Outline each blood parasite and name the species.
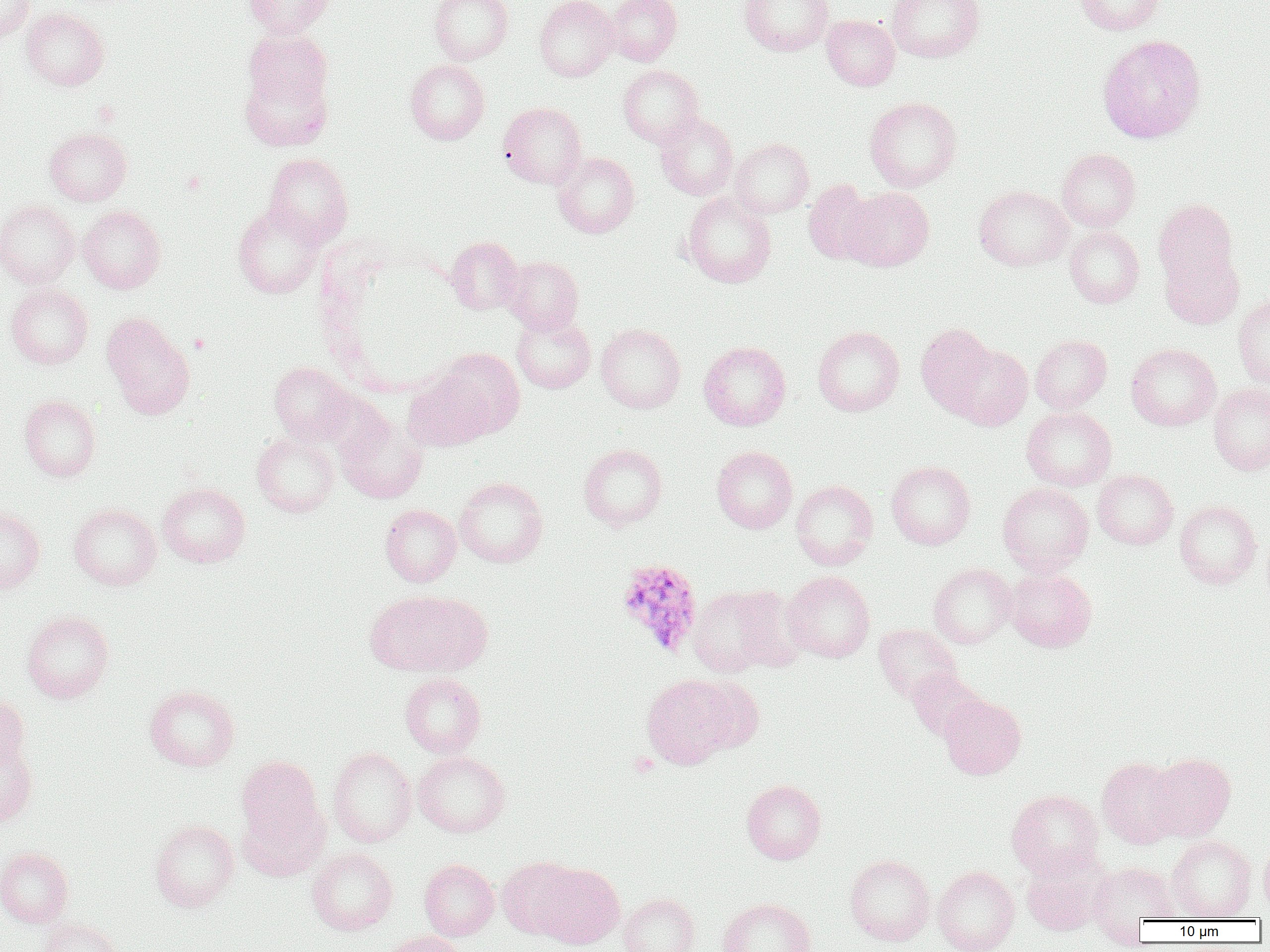
Approximate bounding boxes as (x1,y1)-(x2,y2) corner pairs in pixels.
Plasmodium ovale-infected red blood cells: (617,561)-(704,658).
No Plasmodium falciparum, Plasmodium malariae, Plasmodium vivax, Babesia divergens, or Trypanosoma brucei observed.

{
  "slide_level_diagnosis": "Plasmodium ovale",
  "uninfected_red_blood_cell_locations": "approximate bounding boxes as (x1,y1)-(x2,y2) corner pairs in pixels: (0,0)-(34,41), (244,0)-(332,38), (429,0)-(513,64), (534,0)-(618,81), (605,0)-(682,65), (739,0)-(833,55), (886,0)-(985,62), (1076,0)-(1166,35), (20,7)-(110,91), (822,15)-(899,90), (1097,34)-(1206,143), (405,59)-(490,144), (239,64)-(333,151), (618,64)-(703,147), (865,96)-(962,192), (498,102)-(587,188), (654,112)-(739,200), (44,127)-(132,206), (729,138)-(814,218), (1057,149)-(1140,231), (553,152)-(640,238), (264,153)-(353,245), (803,179)-(877,264), (974,185)-(1073,271), (842,186)-(934,271), (681,192)-(776,287), (1153,199)-(1239,291), (0,200)-(79,288), (233,203)-(323,298), (78,205)-(166,294), (1065,226)-(1144,308), (446,236)-(523,314), (1160,250)-(1243,329), (502,256)-(583,334), (6,283)-(93,369), (1233,294)-(1270,388), (102,313)-(195,418), (511,313)-(595,393), (596,323)-(685,413), (915,323)-(997,416), (813,326)-(904,416), (1030,334)-(1111,413), (698,340)-(791,430), (949,343)-(1032,430), (1126,343)-(1220,430), (435,348)-(525,438), (269,362)-(354,444), (403,371)-(492,451), (1209,383)-(1270,475), (18,395)-(101,481), (1022,407)-(1117,490), (336,414)-(427,503), (252,431)-(339,517), (578,443)-(667,530), (711,446)-(797,533), (886,461)-(976,549), (1093,469)-(1178,549), (454,476)-(548,568), (791,480)-(878,569), (158,482)-(250,567), (998,483)-(1093,575), (1174,500)-(1262,588), (69,502)-(161,590), (380,504)-(461,586), (0,506)-(45,595), (928,563)-(1016,648), (1005,567)-(1096,652), (782,571)-(875,662), (731,584)-(808,671), (688,585)-(785,676), (364,589)-(486,678), (22,610)-(114,703), (874,624)-(961,702), (907,668)-(986,741), (400,673)-(486,757), (642,674)-(739,769), (691,676)-(765,754), (144,684)-(239,771), (0,693)-(30,775), (939,695)-(1026,778), (0,733)-(38,828), (327,746)-(416,847), (413,750)-(510,837), (1146,752)-(1236,841), (236,755)-(326,849), (1097,757)-(1185,849), (741,779)-(826,864), (1007,789)-(1103,878), (237,797)-(329,881), (149,819)-(239,911), (1166,834)-(1257,920), (1259,840)-(1270,915), (0,847)-(73,927), (306,847)-(398,935), (1021,850)-(1111,936), (845,854)-(935,946), (498,856)-(583,939), (419,859)-(499,940), (537,863)-(624,948), (1089,863)-(1180,930), (933,865)-(1020,952), (618,893)-(700,952), (718,898)-(816,952), (39,918)-(126,952), (378,931)-(466,952)",
  "preparation": "thin blood film",
  "platelet_locations": "approximate bounding boxes as (x1,y1)-(x2,y2) corner pairs in pixels: (630,753)-(659,777)",
  "modality": "light microscopy",
  "image_size": "1270×952 pixels",
  "magnification": "1000x",
  "field_of_view": "single"
}